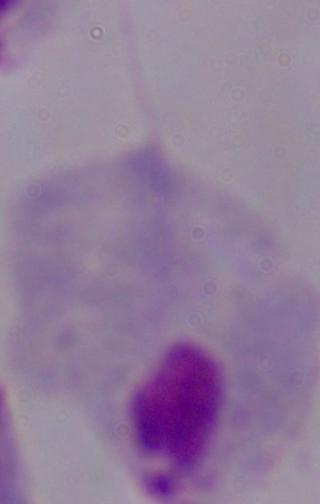
Photomicrograph. 1000x magnification. A trichomonad is shown.